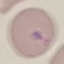

result = negative for malaria parasites
image type = cell patch, automatically extracted from a larger field of view and resized to 64 × 64 pixels
capture = smartphone through the microscope eyepiece
stain = Giemsa
preparation = thin blood film